Classify this cell by malaria status.
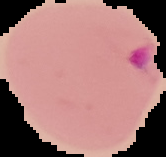

It is parasitized.

{
  "image_type": "segmented cell region with the area outside set to black",
  "image_size": "166×157 pixels",
  "preparation": "thin blood smear"
}